Report the malaria status of this cell.
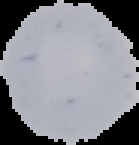
Uninfected.

Summary:
  - Preparation: thin blood film
  - Image size: 139×145 pixels
  - Image type: segmented cell region on a black background